Identify the blood parasite species.
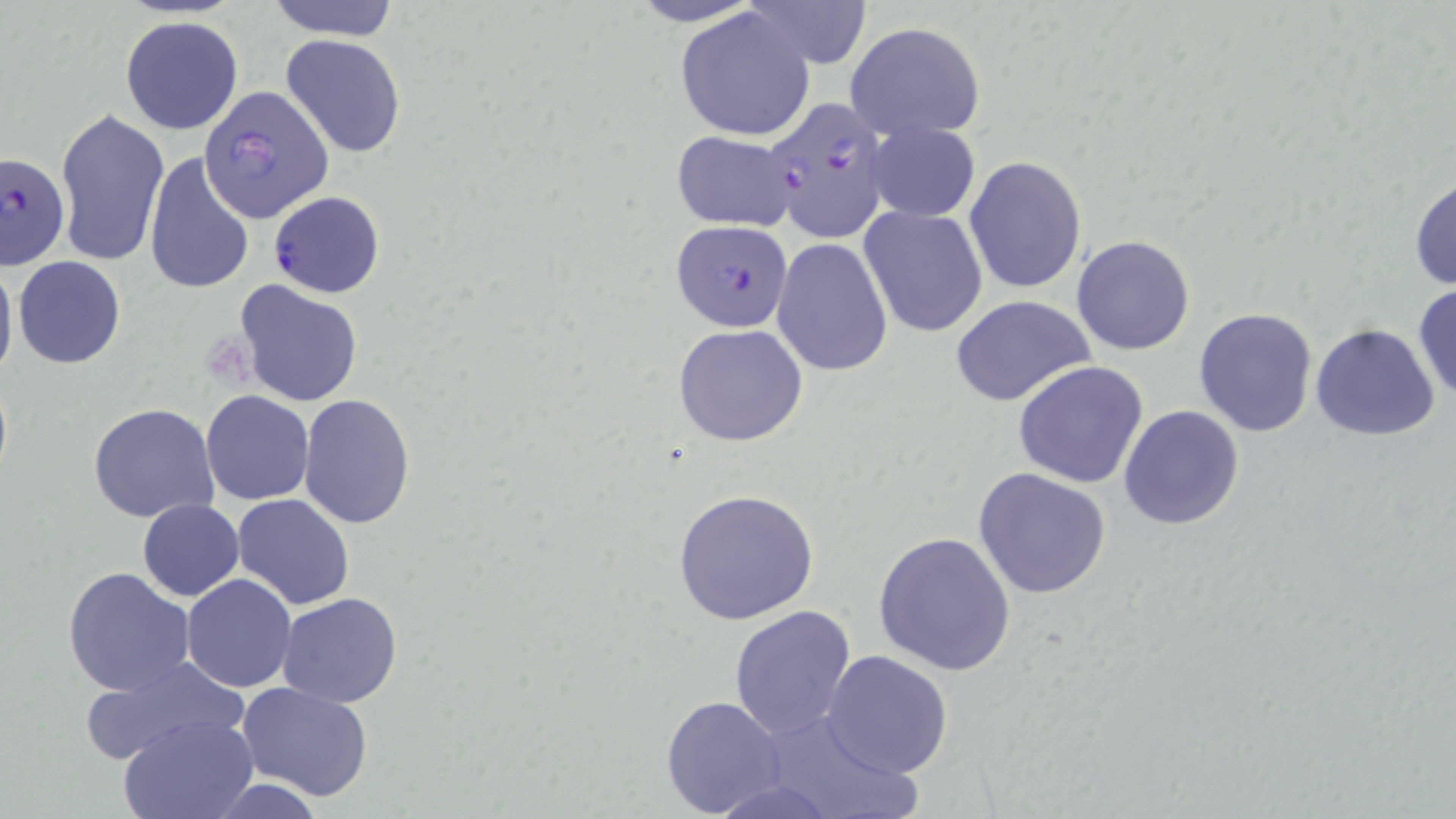

Plasmodium falciparum.

modality = optical microscopy
Plasmodium falciparum-infected red blood cell locations = approximate bounding boxes as (x1,y1)-(x2,y2) corner pairs in pixels: (200,87)-(334,221), (763,96)-(891,244), (1,151)-(70,272), (267,189)-(385,298), (670,218)-(795,331)
magnification = 1000x
preparation = thin blood film
uninfected red blood cell locations = approximate bounding boxes as (x1,y1)-(x2,y2) corner pairs in pixels: (265,0)-(403,41), (621,0)-(771,28), (740,0)-(873,69), (675,6)-(817,141), (119,16)-(244,136), (845,21)-(986,142), (280,34)-(407,158), (54,106)-(169,266), (865,121)-(982,223), (669,130)-(801,231), (144,152)-(255,295), (964,156)-(1087,295), (1409,173)-(1456,292), (858,206)-(988,338), (1071,234)-(1196,356), (771,239)-(892,377), (0,255)-(18,385), (13,257)-(125,369), (234,279)-(364,407), (1412,285)-(1456,404), (948,293)-(1097,407), (1193,309)-(1318,436), (674,323)-(807,447), (1309,323)-(1442,442), (1013,361)-(1148,488), (200,391)-(314,506), (299,393)-(416,527), (89,403)-(220,522), (1119,405)-(1246,531), (213,418)-(339,571), (973,468)-(1111,599), (673,489)-(819,625), (232,494)-(355,610), (137,499)-(245,601), (873,529)-(1016,675), (63,566)-(195,696), (181,574)-(297,692), (278,593)-(404,708), (728,605)-(857,741), (821,649)-(953,778), (76,655)-(249,765), (235,680)-(374,802), (660,695)-(787,817), (757,708)-(920,819), (119,714)-(260,819), (204,777)-(330,817)
stain = May-Grünwald-Giemsa
image size = 1456×819 pixels
field of view = single